Report the malaria status of this cell.
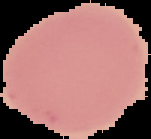
Uninfected.

From a thin blood film. Segmented cell region on a black background. Image is 151×139 pixels.